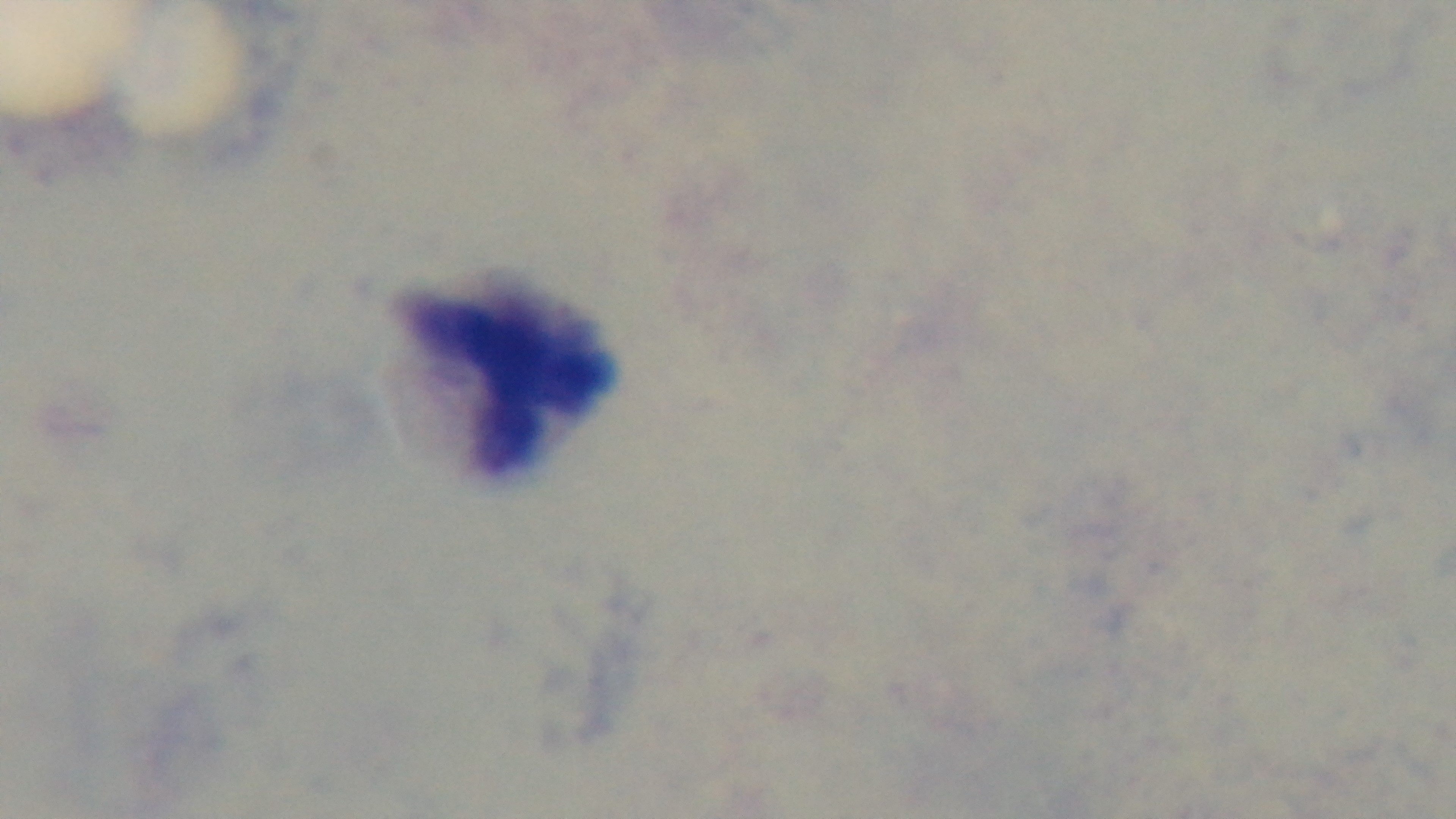

Summary:
  - Modality: light microscopy
  - Preparation: thick
  - Capture: mounted 4K digital camera
  - Stain: Giemsa
  - Objective: 100x oil immersion
  - Malaria status: negative
  - Field of view: one from the slide